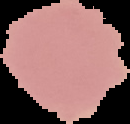
Summary:
  - Image size: 130×124 pixels
  - Image type: segmented cell region on a black background
  - Malaria status: uninfected
  - Preparation: thin blood film